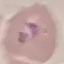
Summary:
  - Malaria status: parasitized
  - Preparation: thin blood smear
  - Capture: smartphone through the microscope eyepiece
  - Stain: Giemsa
  - Image type: cell patch, automatically extracted from a larger field of view and resized to 64 × 64 pixels